Point out each Plasmodium parasite.
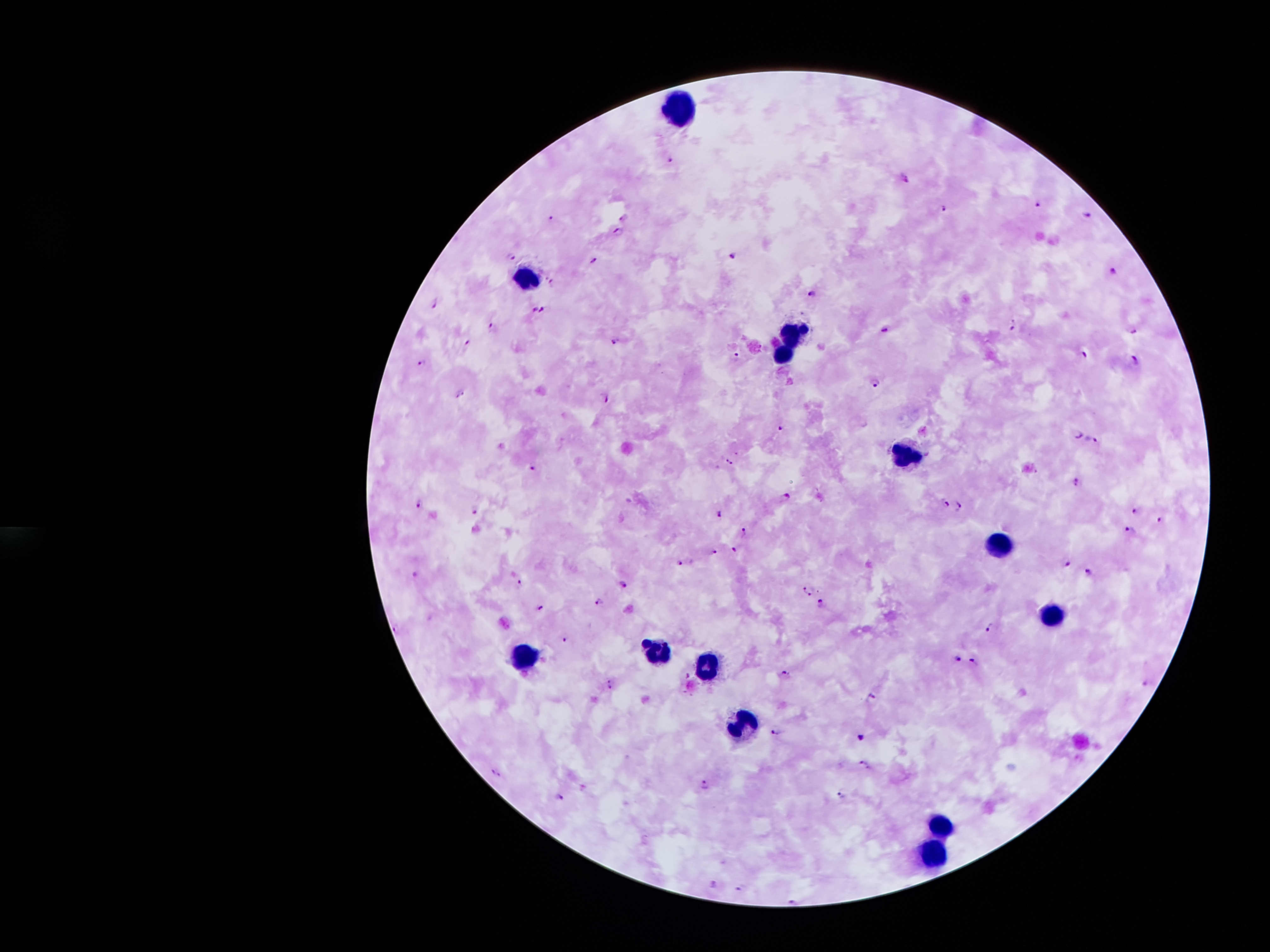
Approximate centers as (x, y) in pixels.
Plasmodium parasites: (671, 158), (904, 181), (1038, 204), (945, 207), (1087, 213), (622, 216), (550, 217), (619, 230), (733, 254), (511, 255), (595, 260), (1115, 272), (552, 284), (813, 292), (433, 303), (546, 309), (535, 310), (1014, 325), (887, 329), (495, 330), (1135, 332), (618, 342), (469, 344), (1087, 356), (735, 358), (1135, 361), (424, 365), (877, 382), (462, 394), (607, 398), (781, 428), (1079, 435), (1091, 442), (730, 461), (532, 467), (1077, 482), (786, 498), (947, 501), (421, 505), (961, 505), (476, 510), (1135, 510), (721, 515), (1160, 520), (1129, 532), (744, 533), (734, 548), (715, 552), (1069, 563), (682, 564), (1089, 571), (416, 573), (521, 582), (623, 586), (809, 591), (599, 603), (822, 604), (540, 609), (992, 627), (397, 628), (563, 639), (956, 658), (971, 662), (787, 674), (609, 683), (1147, 683), (873, 697), (776, 732), (862, 736), (863, 763), (496, 772), (705, 785), (842, 793), (561, 797), (713, 884), (743, 887), (794, 899).

Summary:
  - Leukocyte locations: (677, 104), (530, 279), (792, 328), (783, 353), (905, 451), (993, 541), (1048, 612), (660, 655), (523, 658), (706, 667), (743, 723), (939, 819), (930, 850)
  - Image size: 1270×952 pixels
  - Magnification: 100x
  - Patient malaria status: infected with Plasmodium falciparum
  - Stain: Giemsa
  - Field of view: single
  - Preparation: thick peripheral-blood smear
  - Capture: smartphone through the microscope eyepiece